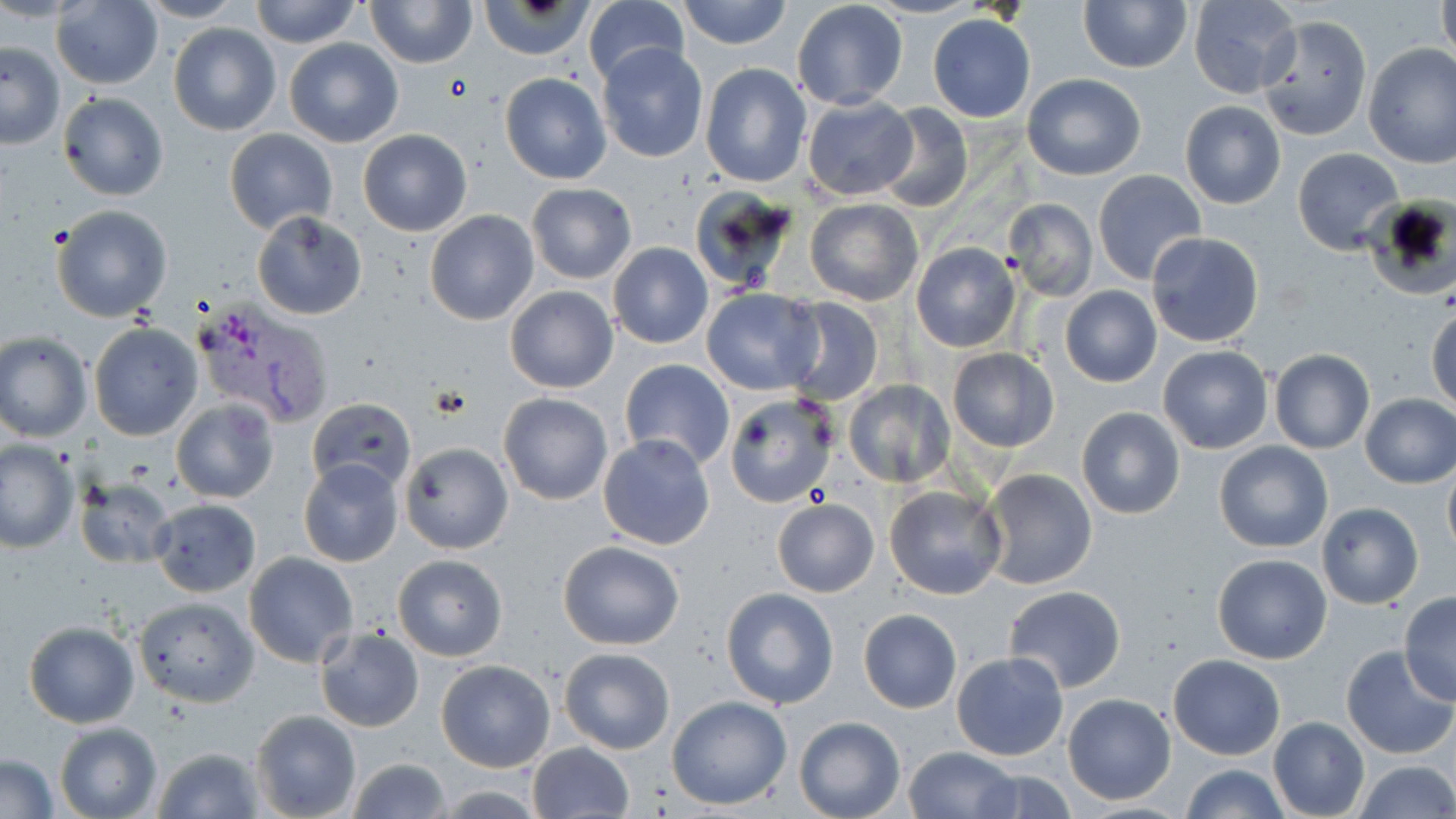
Summary:
  - Coordinate format: approximate bounding boxes as (x1,y1)-(x2,y2) corner pairs in pixels
  - Uninfected red blood cell locations: (249,0)-(362,49), (364,0)-(477,68), (583,0)-(689,88), (677,0)-(791,50), (867,0)-(982,20), (1080,0)-(1192,73), (1188,0)-(1301,98), (135,1)-(244,24), (791,1)-(908,110), (1437,1)-(1456,62), (50,2)-(165,88), (482,2)-(591,59), (928,14)-(1035,122), (1257,16)-(1372,141), (168,23)-(281,135), (284,39)-(403,148), (1,42)-(66,150), (1362,42)-(1456,167), (597,44)-(708,162), (700,62)-(810,188), (499,72)-(611,184), (1021,72)-(1146,180), (58,91)-(169,201), (802,95)-(919,202), (1180,101)-(1286,210), (874,103)-(973,214), (223,128)-(338,235), (359,129)-(472,237), (1293,147)-(1405,257), (1092,169)-(1207,284), (525,182)-(637,284), (688,186)-(800,297), (1363,197)-(1455,301), (1002,198)-(1098,301), (805,199)-(923,306), (50,203)-(173,322), (251,210)-(368,320), (424,210)-(540,326), (1146,231)-(1265,349), (609,242)-(713,348), (911,243)-(1021,353), (505,285)-(618,393), (1059,286)-(1162,387), (701,287)-(824,395), (780,297)-(885,406), (1428,307)-(1455,413), (89,322)-(203,441), (0,331)-(91,442), (1158,345)-(1273,454), (947,348)-(1059,452), (1270,349)-(1374,453), (620,358)-(735,471), (844,380)-(956,487), (1360,392)-(1456,488), (498,393)-(614,506), (727,393)-(841,508), (170,398)-(279,504), (307,399)-(415,493), (1076,406)-(1185,520), (598,435)-(716,551), (1,439)-(78,552), (399,441)-(513,554), (1213,441)-(1333,553), (298,459)-(403,568), (1442,461)-(1456,558), (978,468)-(1100,591), (74,476)-(177,568), (884,484)-(1007,600), (148,498)-(260,597), (772,498)-(879,598), (1316,502)-(1424,609), (557,539)-(686,651), (243,553)-(358,669), (1212,553)-(1332,664), (393,554)-(507,661), (1003,585)-(1126,693), (722,587)-(839,710), (1399,593)-(1456,705), (132,596)-(258,706), (858,610)-(962,712), (23,619)-(139,728), (314,626)-(424,732), (1341,646)-(1454,759), (559,648)-(675,752), (951,652)-(1069,761), (1168,653)-(1285,760), (435,659)-(556,772), (1063,694)-(1175,803), (667,695)-(791,810), (250,710)-(362,819), (793,717)-(904,819), (1267,717)-(1369,818), (53,721)-(163,819), (527,742)-(634,818), (151,744)-(263,818), (903,747)-(1020,819), (1,754)-(60,817), (344,757)-(453,819), (1350,759)-(1456,818), (1182,764)-(1289,819), (969,766)-(1075,819), (426,785)-(553,817)
  - Plasmodium vivax-infected red blood cell locations: (196,296)-(335,427)
  - Slide-level diagnosis: Plasmodium vivax
  - Preparation: thin blood smear
  - Magnification: 1000x
  - Field of view: one of a larger specimen
  - Stain: May-Grünwald-Giemsa
  - Image size: 1456×819 pixels
  - Modality: optical microscopy